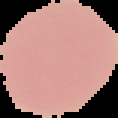
Summary:
  - Result: negative for malaria parasites
  - Image size: 118×118 pixels
  - Image type: segmented cell region with the area outside set to black
  - Preparation: thin blood film